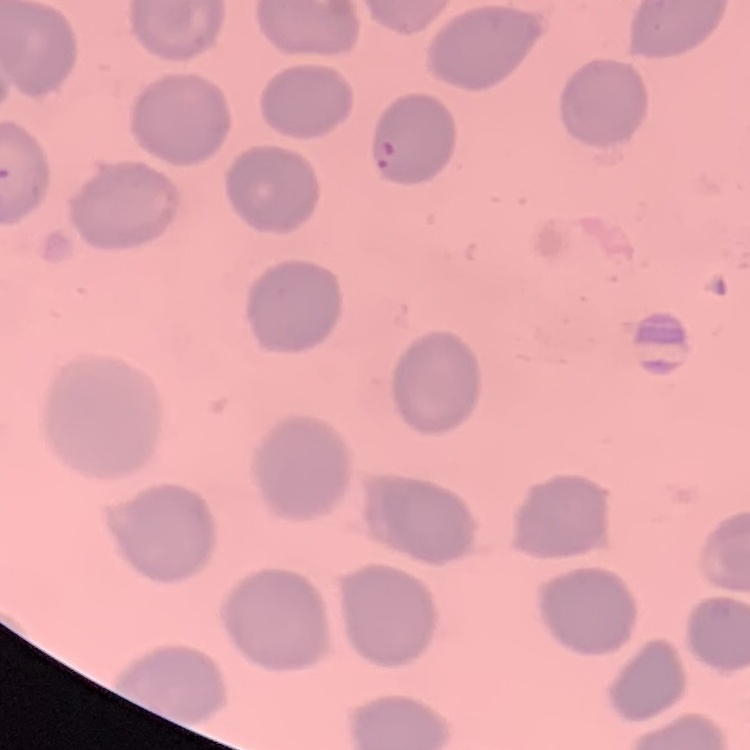 The erythrocytes show no rouleaux formation. Square crop of a larger photomicrograph. Thin peripheral smear. Stained with either Field's or Giemsa.